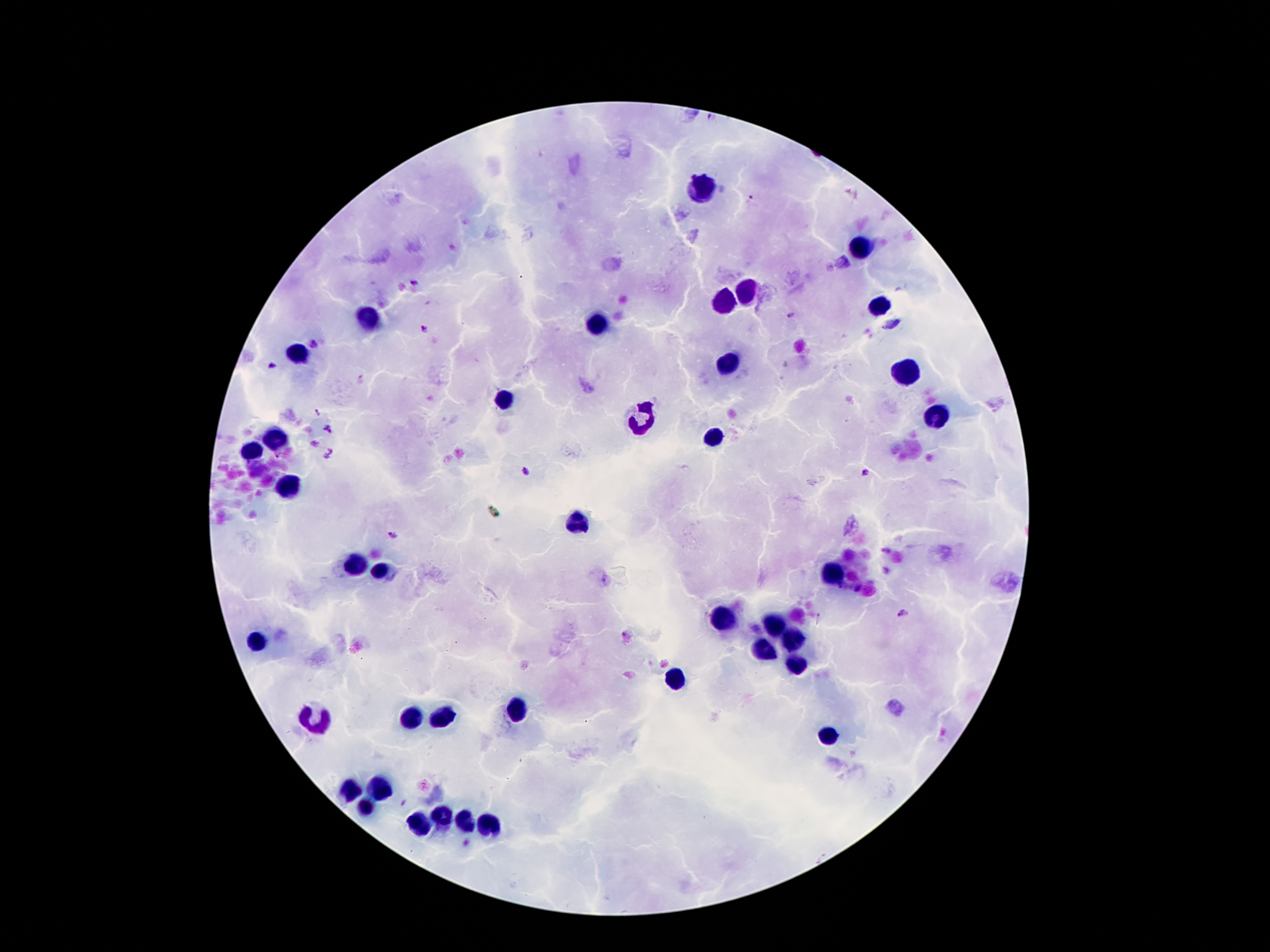
Approximate centers as {x, y} in pixels.
Summary:
  - Plasmodium parasite locations: {751, 199}, {414, 283}, {790, 314}, {423, 328}, {314, 343}, {271, 366}, {317, 412}, {329, 428}, {277, 454}, {526, 471}, {865, 472}, {392, 535}, {902, 615}, {625, 636}
  - Leukocyte locations: {706, 188}, {859, 248}, {749, 291}, {722, 298}, {878, 303}, {370, 320}, {602, 322}, {298, 354}, {727, 364}, {904, 370}, {502, 400}, {644, 414}, {936, 416}, {274, 438}, {715, 438}, {250, 454}, {286, 486}, {578, 524}, {355, 565}, {381, 570}, {835, 570}, {717, 620}, {772, 625}, {257, 639}, {792, 639}, {761, 647}, {796, 664}, {674, 680}, {516, 711}, {408, 718}, {316, 719}, {441, 719}, {828, 736}, {381, 790}, {350, 791}, {367, 807}, {444, 815}, {465, 822}, {489, 824}, {420, 827}
  - Field of view: single
  - Stain: Giemsa
  - Image size: 1270×952 pixels
  - Patient malaria status: infected with Plasmodium falciparum
  - Magnification: 100x
  - Preparation: thick peripheral-blood smear
  - Capture: smartphone camera through the microscope eyepiece